State which parasite is depicted.
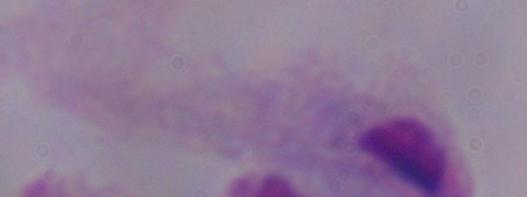

This is a trichomonad.

{
  "modality": "micrograph",
  "magnification": "1000x"
}